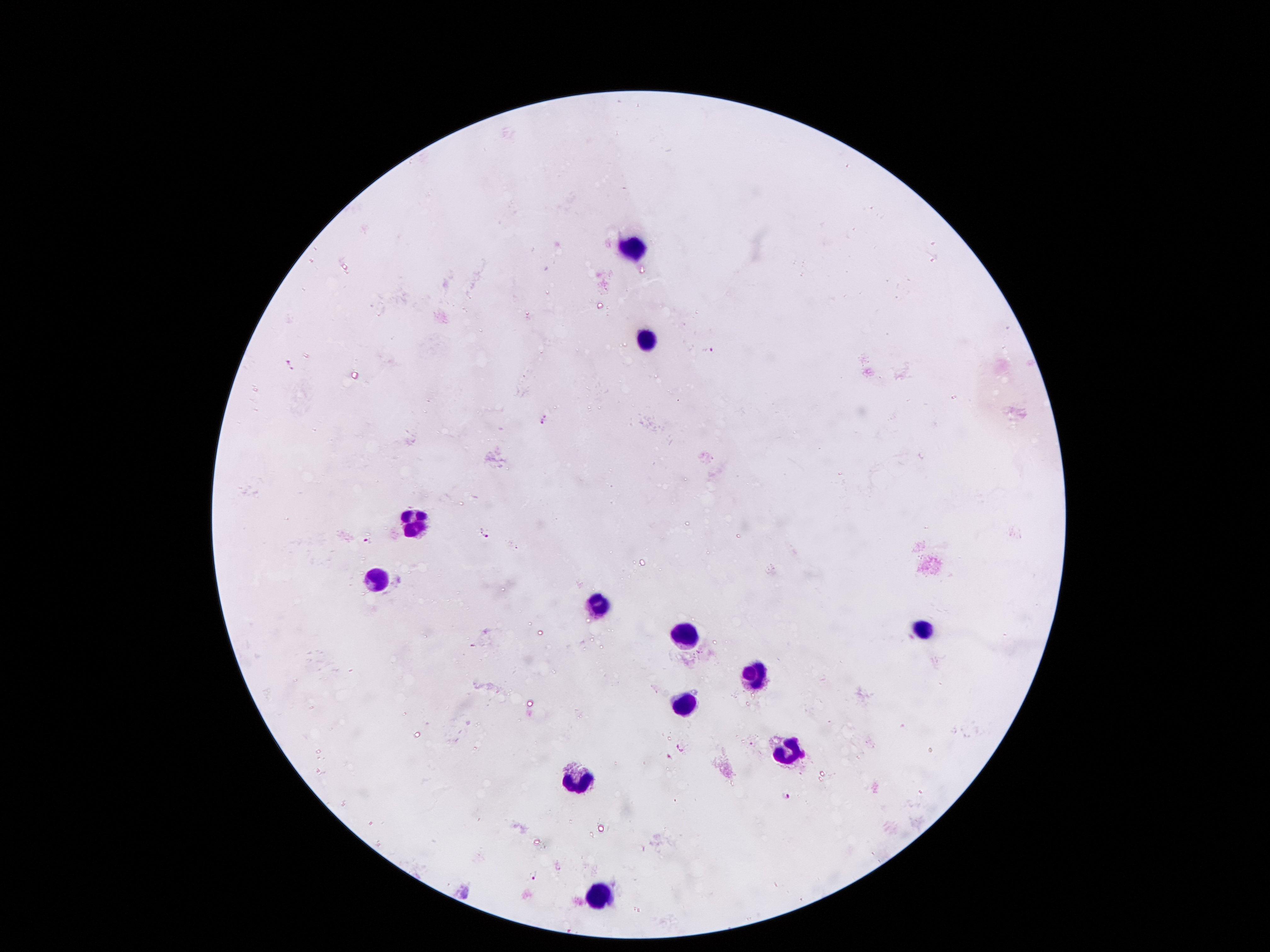

coordinate format = approximate centers as (x, y) in pixels
Plasmodium parasite locations = (711, 348), (290, 365), (545, 418), (485, 533), (366, 540), (680, 746), (670, 756), (786, 795), (532, 874)
leukocyte locations = (638, 251), (643, 339), (409, 524), (374, 577), (597, 604), (926, 628), (686, 633), (757, 671), (681, 707), (785, 753), (572, 779), (602, 897)
magnification = 100x
stain = Giemsa
patient malaria status = infected with Plasmodium falciparum
capture = smartphone through the microscope eyepiece
preparation = thick blood film
field of view = single
image size = 1270×952 pixels